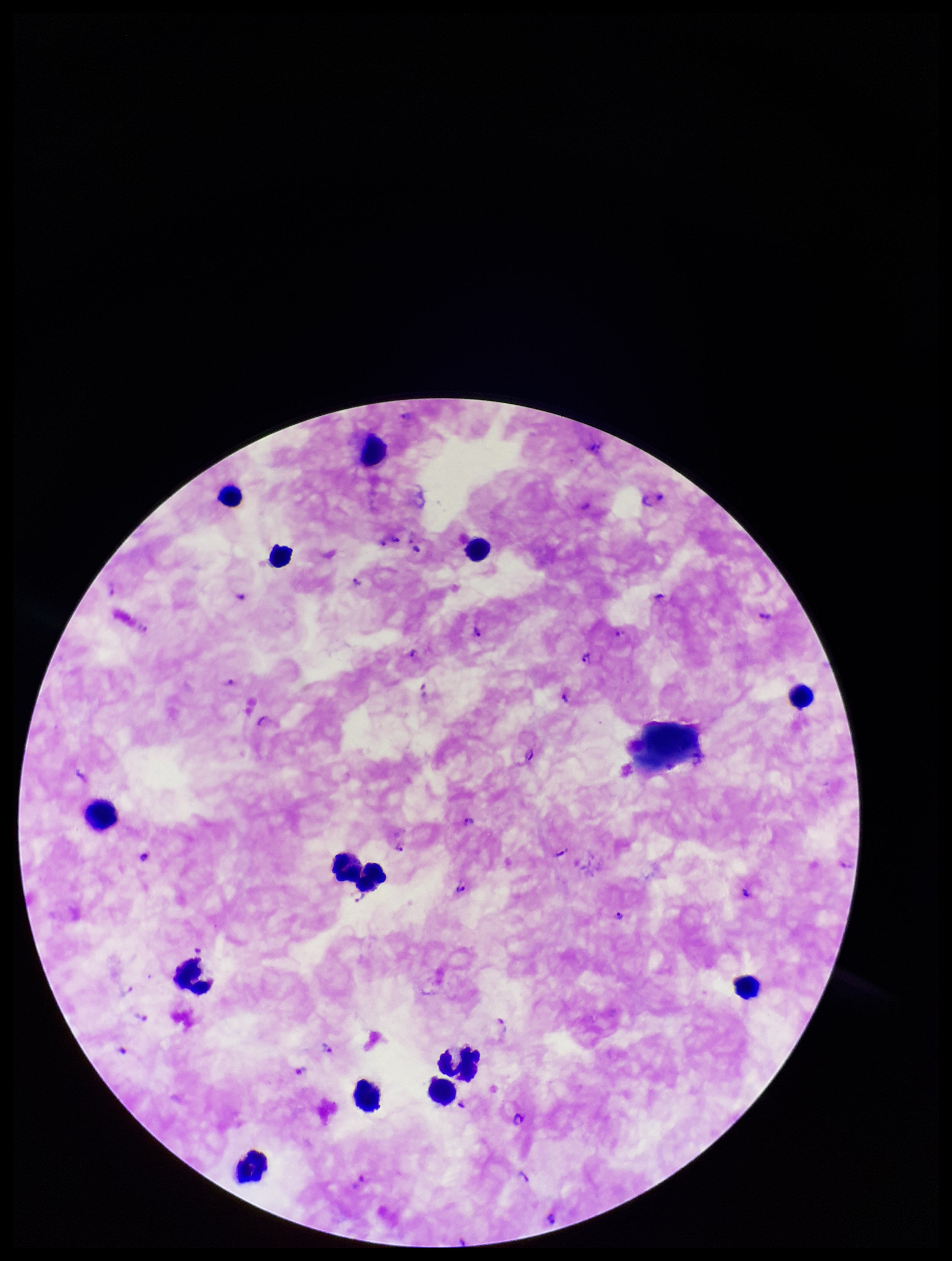
Summary:
  - Plasmodium parasites: detected
  - Patient malaria status: infected
  - Stain: Giemsa
  - Parasite count: 27
  - Capture: smartphone photograph through the microscope eyepiece
  - Preparation: thick blood smear
  - Leukocyte count: 14
  - Field of view: single
  - Image size: 952×1261 pixels
  - Species reported for this patient: Plasmodium falciparum